Assess the morphology of the red blood cells.
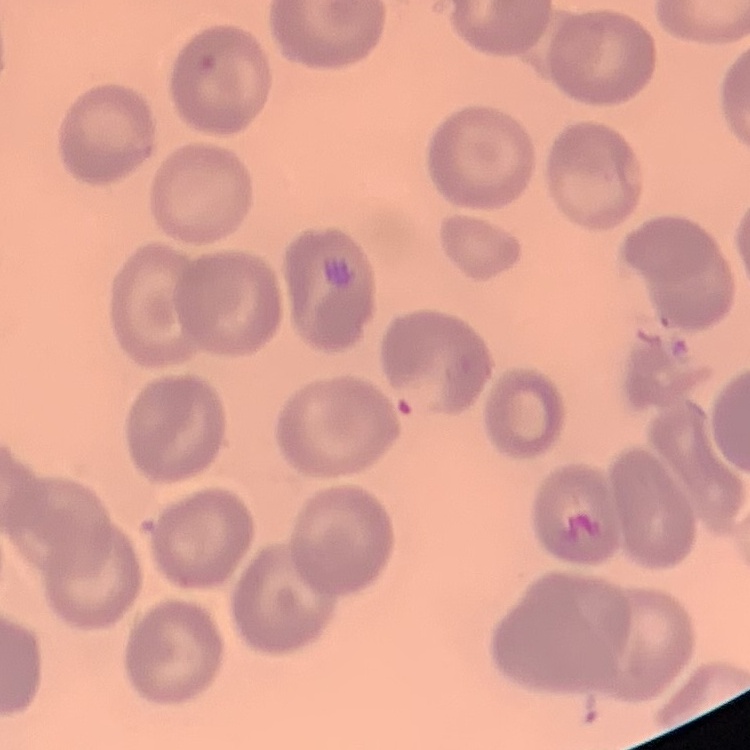
They show no rouleaux formation.

stain = Field's or Giemsa
image type = one tile cut from a larger photomicrograph
preparation = thin blood smear